Classify this cell by malaria status.
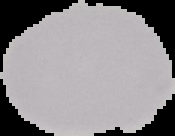

Uninfected.

Summary:
  - Image type: segmented cell region with the area outside set to black
  - Image size: 175×136 pixels
  - Preparation: thin blood smear